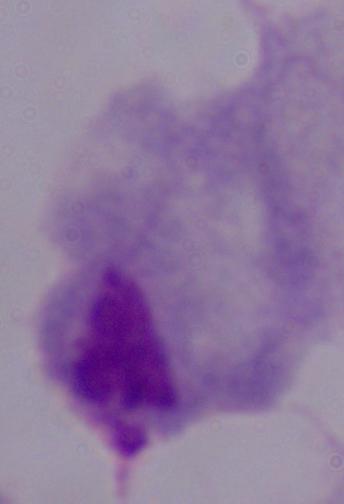

identification: trichomonad
modality: micrograph
magnification: 1000x